Give the position of every leukocyte visible.
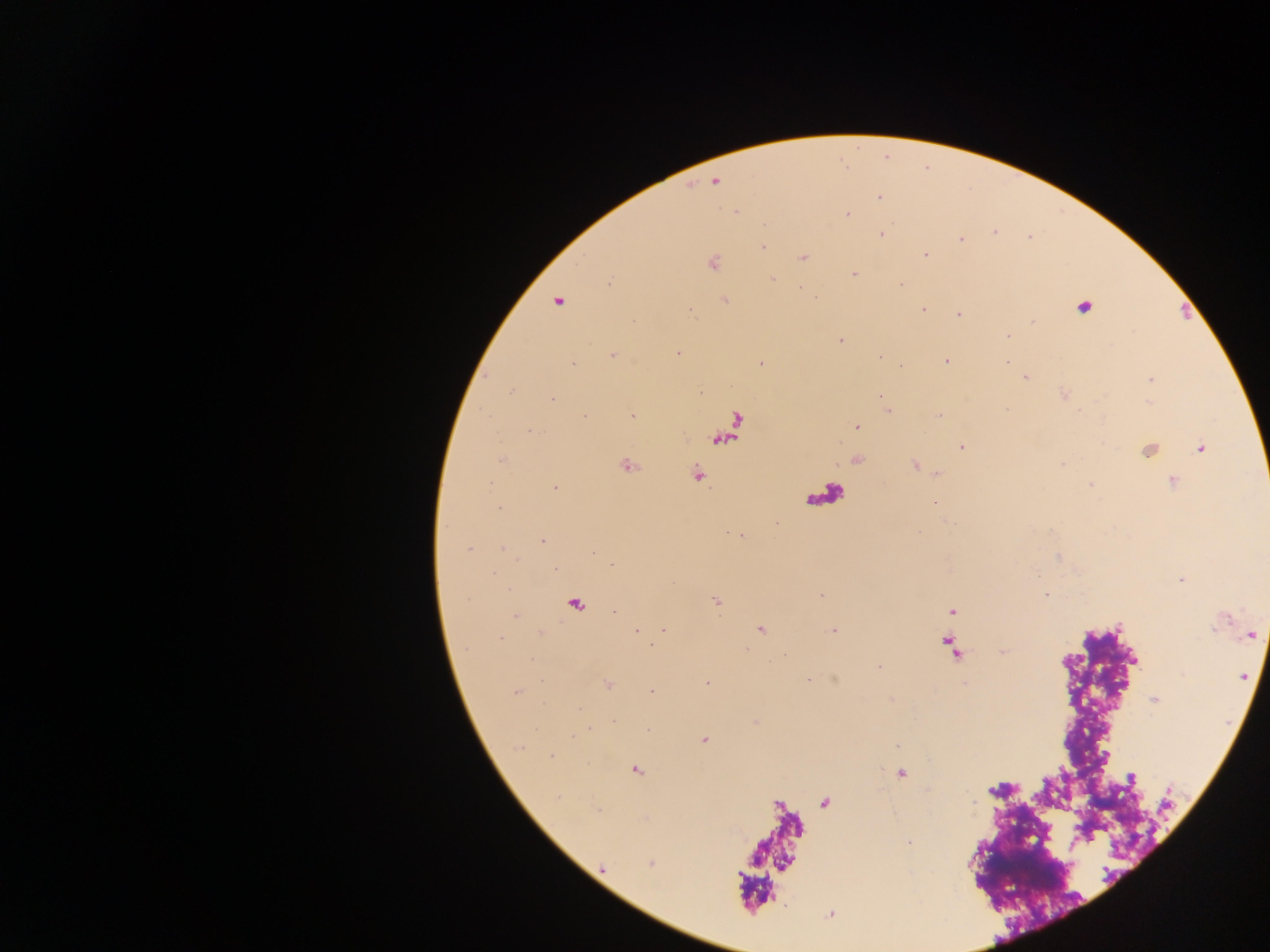
No leukocytes observed.

Approximate centers as (x, y) in pixels. Plasmodium parasite locations: (715, 182), (879, 197), (736, 211), (847, 214), (764, 223), (995, 232), (881, 233), (960, 239), (763, 247), (925, 254), (803, 257), (711, 262), (853, 274), (772, 280), (609, 283), (900, 283), (798, 289), (725, 300), (557, 301), (1083, 306), (922, 309), (958, 314), (1008, 335), (840, 341), (677, 353), (613, 355), (945, 360), (573, 362), (760, 363), (1025, 376), (1150, 379), (510, 391), (1064, 394), (880, 395), (551, 399), (887, 409), (631, 415), (939, 415), (583, 417), (857, 427), (528, 430), (962, 446), (1200, 447), (1148, 449), (502, 459), (857, 459), (626, 465), (914, 465), (936, 473), (696, 475), (1172, 480), (555, 487), (934, 502), (740, 534), (542, 540), (469, 548), (503, 549), (1181, 579), (1046, 594), (821, 596), (716, 601), (574, 604), (615, 612), (515, 615), (759, 628), (833, 629), (636, 630), (663, 630), (1251, 634), (607, 684), (517, 691), (652, 691), (1155, 700), (704, 739), (635, 769), (899, 774), (651, 863), (602, 868), (829, 914). Thick blood film. Photographed through a microscope with a mobile-phone camera. Collected in Ghana. One field of view. Image is 1270×952 pixels.